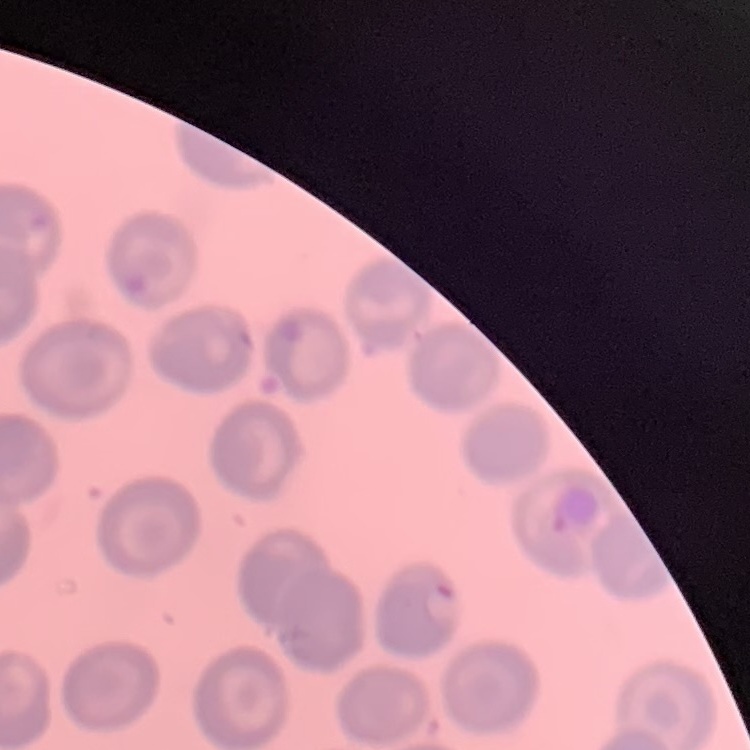

Summary:
  - Red blood cell morphology: no rouleaux formation
  - Preparation: thin peripheral smear
  - Image type: one tile cut from a larger photomicrograph
  - Stain: Field's or Giemsa